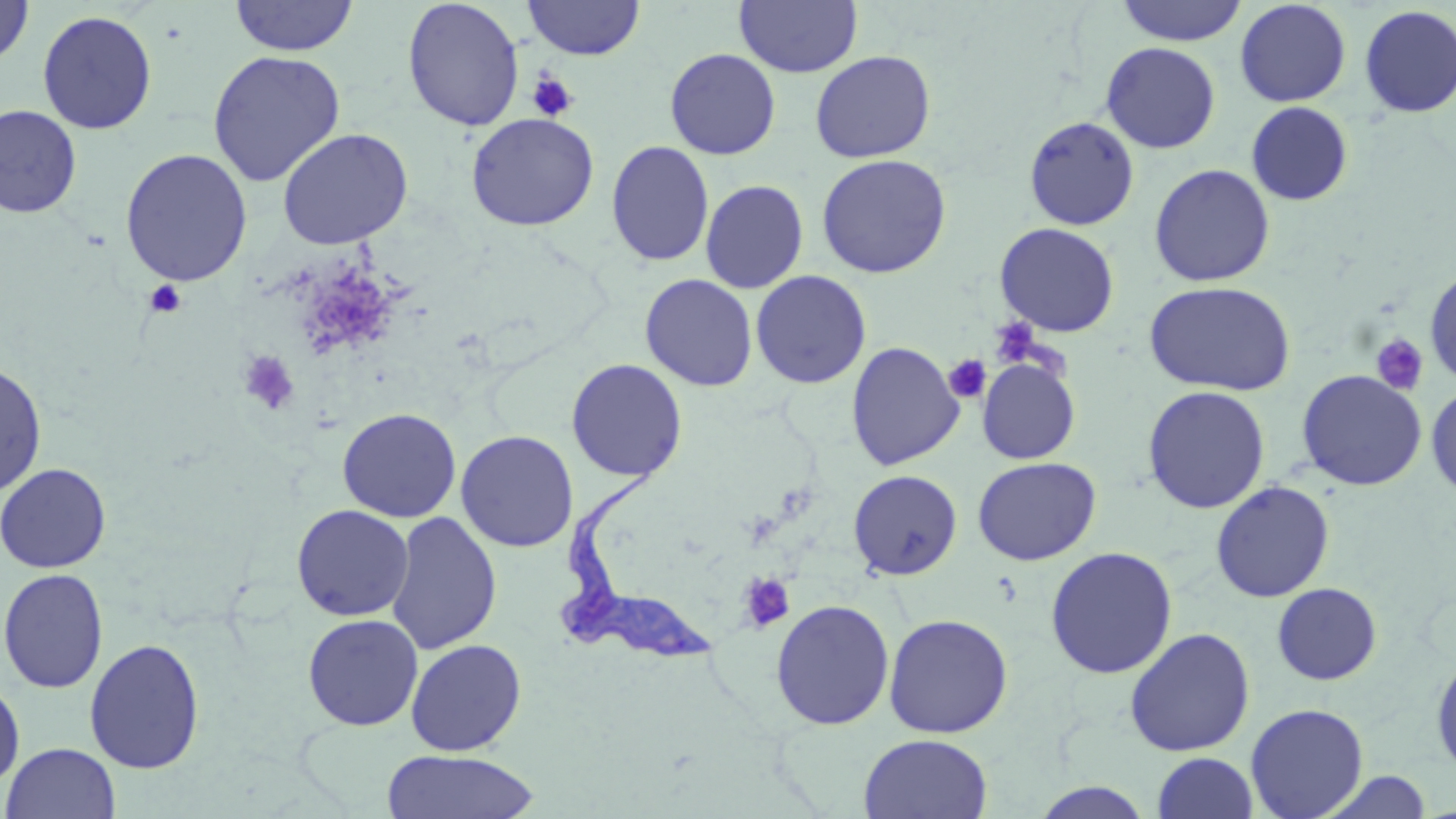
Summary:
  - Coordinate format: approximate bounding boxes as (x1, y1, x2, y2) in pixels
  - Uninfected red blood cell locations: (1, 0, 35, 68), (228, 0, 358, 57), (402, 0, 525, 131), (523, 0, 645, 60), (734, 0, 862, 78), (1115, 0, 1248, 46), (1234, 1, 1351, 106), (1358, 5, 1456, 118), (36, 9, 158, 134), (1101, 42, 1220, 154), (664, 48, 781, 160), (207, 49, 346, 187), (810, 50, 935, 163), (1246, 101, 1353, 206), (0, 104, 82, 218), (465, 112, 599, 231), (1023, 116, 1140, 231), (277, 127, 413, 250), (606, 140, 715, 267), (119, 148, 253, 287), (815, 153, 952, 279), (1149, 163, 1275, 287), (700, 179, 808, 294), (994, 222, 1120, 337), (1424, 267, 1456, 389), (750, 270, 871, 389), (639, 273, 758, 392), (1143, 280, 1297, 396), (846, 341, 964, 471), (566, 358, 688, 483), (977, 359, 1080, 465), (0, 361, 48, 496), (1295, 369, 1427, 491), (1426, 383, 1456, 499), (1142, 385, 1271, 514), (337, 407, 461, 522), (456, 430, 579, 553), (972, 456, 1101, 566), (0, 462, 112, 573), (848, 469, 963, 580), (1211, 480, 1334, 602), (291, 504, 414, 621), (386, 511, 502, 656), (1045, 546, 1178, 679), (1, 568, 109, 693), (1271, 582, 1382, 685), (770, 599, 895, 730), (302, 613, 423, 731), (883, 613, 1013, 738), (1124, 627, 1255, 757), (84, 637, 205, 774), (406, 639, 527, 756), (1430, 654, 1456, 777), (0, 677, 25, 791), (1245, 703, 1369, 818), (858, 733, 993, 819), (2, 742, 120, 818), (380, 749, 542, 819), (1152, 751, 1259, 819), (1318, 770, 1433, 818), (1028, 781, 1156, 818)
  - Platelet locations: (527, 70, 579, 122), (144, 280, 187, 318), (989, 319, 1041, 367), (1370, 333, 1429, 396), (238, 350, 300, 415), (944, 355, 990, 403), (738, 573, 795, 633)
  - Trypanosoma brucei locations: (551, 456, 722, 669)
  - Slide-level diagnosis: Trypanosoma brucei
  - Stain: May-Grünwald-Giemsa
  - Magnification: 1000x
  - Preparation: thin blood film
  - Modality: optical microscopy
  - Image size: 1456×819 pixels
  - Field of view: single